Outline each blood parasite and name the species.
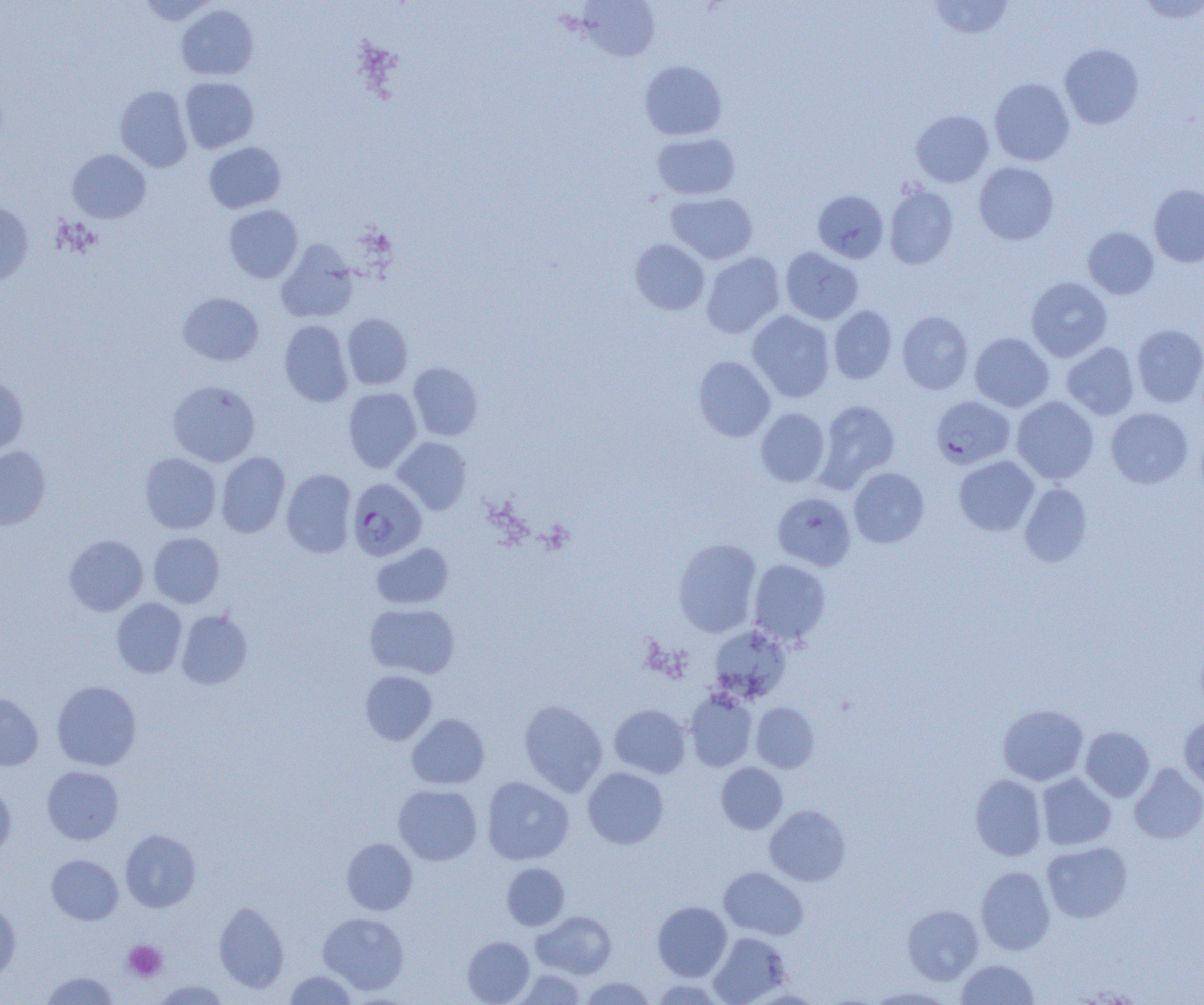

Approximate bounding boxes as named x1/y1/x2/y2 corners in pixels.
Plasmodium falciparum-infected red blood cells: (x1=931, y1=395, x2=1015, y2=469), (x1=347, y1=478, x2=427, y2=561).
No Plasmodium ovale, Plasmodium malariae, Plasmodium vivax, Babesia divergens, or Trypanosoma brucei observed.

Platelet locations: (x1=123, y1=940, x2=167, y2=981). Uninfected red blood cell locations: (x1=138, y1=0, x2=219, y2=25), (x1=577, y1=0, x2=660, y2=61), (x1=1137, y1=0, x2=1204, y2=23), (x1=927, y1=1, x2=1014, y2=40), (x1=176, y1=4, x2=259, y2=80), (x1=1059, y1=43, x2=1144, y2=129), (x1=639, y1=60, x2=727, y2=140), (x1=180, y1=77, x2=259, y2=154), (x1=989, y1=78, x2=1075, y2=165), (x1=114, y1=85, x2=193, y2=172), (x1=911, y1=110, x2=994, y2=187), (x1=652, y1=132, x2=740, y2=200), (x1=204, y1=142, x2=286, y2=213), (x1=67, y1=149, x2=151, y2=223), (x1=974, y1=162, x2=1059, y2=245), (x1=884, y1=184, x2=959, y2=269), (x1=1149, y1=184, x2=1204, y2=267), (x1=813, y1=189, x2=889, y2=263), (x1=666, y1=192, x2=757, y2=264), (x1=0, y1=201, x2=33, y2=286), (x1=224, y1=205, x2=303, y2=283), (x1=1083, y1=227, x2=1159, y2=299), (x1=276, y1=239, x2=359, y2=323), (x1=630, y1=239, x2=710, y2=315), (x1=781, y1=247, x2=863, y2=325), (x1=701, y1=252, x2=785, y2=338), (x1=1026, y1=277, x2=1112, y2=361), (x1=178, y1=292, x2=264, y2=365), (x1=828, y1=305, x2=897, y2=384), (x1=747, y1=311, x2=835, y2=402), (x1=897, y1=311, x2=973, y2=394), (x1=342, y1=313, x2=413, y2=389), (x1=279, y1=320, x2=353, y2=407), (x1=1132, y1=324, x2=1204, y2=407), (x1=970, y1=333, x2=1054, y2=412), (x1=1062, y1=342, x2=1140, y2=420), (x1=693, y1=356, x2=775, y2=442), (x1=409, y1=362, x2=483, y2=440), (x1=0, y1=375, x2=28, y2=455), (x1=168, y1=380, x2=261, y2=466), (x1=343, y1=387, x2=421, y2=472), (x1=1012, y1=396, x2=1099, y2=484), (x1=816, y1=400, x2=900, y2=490), (x1=1106, y1=407, x2=1193, y2=488), (x1=755, y1=408, x2=830, y2=487), (x1=392, y1=437, x2=471, y2=514), (x1=0, y1=446, x2=50, y2=529), (x1=216, y1=452, x2=290, y2=537), (x1=140, y1=453, x2=221, y2=534), (x1=954, y1=456, x2=1039, y2=536), (x1=848, y1=467, x2=929, y2=548), (x1=281, y1=469, x2=357, y2=558), (x1=1019, y1=483, x2=1093, y2=567), (x1=772, y1=492, x2=856, y2=570), (x1=148, y1=532, x2=225, y2=608), (x1=64, y1=535, x2=148, y2=616), (x1=673, y1=538, x2=762, y2=637), (x1=371, y1=543, x2=454, y2=609), (x1=748, y1=559, x2=831, y2=645), (x1=112, y1=598, x2=188, y2=677), (x1=364, y1=603, x2=460, y2=678), (x1=176, y1=609, x2=252, y2=689), (x1=709, y1=624, x2=791, y2=702), (x1=360, y1=670, x2=437, y2=745), (x1=52, y1=680, x2=142, y2=771), (x1=684, y1=690, x2=757, y2=771), (x1=0, y1=691, x2=43, y2=771), (x1=518, y1=700, x2=607, y2=796), (x1=751, y1=702, x2=819, y2=773), (x1=609, y1=704, x2=691, y2=777), (x1=998, y1=704, x2=1088, y2=785), (x1=406, y1=713, x2=489, y2=789), (x1=1179, y1=715, x2=1204, y2=795), (x1=1080, y1=726, x2=1154, y2=801), (x1=716, y1=762, x2=787, y2=834), (x1=1129, y1=763, x2=1204, y2=844), (x1=42, y1=766, x2=124, y2=844), (x1=583, y1=767, x2=668, y2=849), (x1=1037, y1=773, x2=1116, y2=850), (x1=970, y1=775, x2=1046, y2=860), (x1=481, y1=776, x2=574, y2=865), (x1=0, y1=783, x2=16, y2=858), (x1=393, y1=784, x2=482, y2=865), (x1=765, y1=804, x2=851, y2=886), (x1=120, y1=829, x2=200, y2=912), (x1=341, y1=838, x2=417, y2=914), (x1=1042, y1=841, x2=1132, y2=923), (x1=46, y1=854, x2=123, y2=924), (x1=501, y1=863, x2=569, y2=930), (x1=976, y1=866, x2=1055, y2=954), (x1=719, y1=867, x2=808, y2=940), (x1=0, y1=894, x2=21, y2=981), (x1=213, y1=901, x2=289, y2=993), (x1=652, y1=901, x2=732, y2=981), (x1=903, y1=905, x2=983, y2=985), (x1=532, y1=911, x2=616, y2=979), (x1=318, y1=912, x2=409, y2=995), (x1=708, y1=932, x2=791, y2=1004), (x1=462, y1=936, x2=534, y2=1004), (x1=956, y1=959, x2=1039, y2=1004), (x1=513, y1=970, x2=585, y2=1004), (x1=41, y1=971, x2=119, y2=1005), (x1=284, y1=971, x2=356, y2=1004), (x1=579, y1=977, x2=656, y2=1004), (x1=649, y1=979, x2=725, y2=1004), (x1=152, y1=980, x2=231, y2=1004), (x1=866, y1=986, x2=955, y2=1004). Slide-level diagnosis: Plasmodium falciparum. One field of a larger specimen. Thin blood smear. Image is 1204×1005 pixels. Light microscopy. 1000x magnification.